Give the position of every Plasmodium parasite.
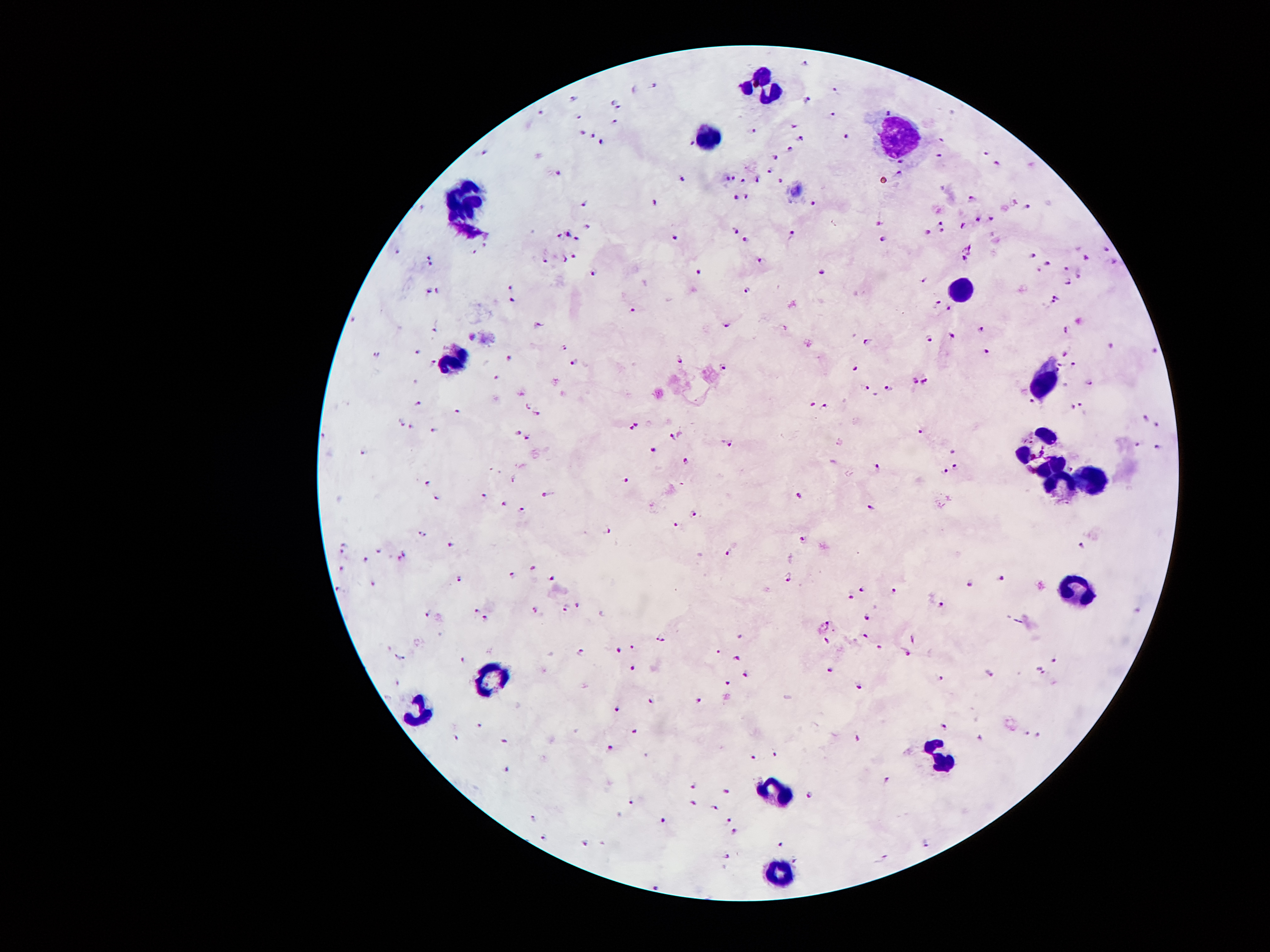

Approximate centers as {x, y} in pixels.
Plasmodium parasites: {805, 64}, {656, 86}, {635, 88}, {834, 89}, {575, 97}, {614, 100}, {808, 100}, {621, 108}, {541, 113}, {578, 114}, {834, 115}, {616, 120}, {583, 129}, {794, 129}, {752, 131}, {592, 134}, {847, 137}, {602, 141}, {801, 141}, {940, 141}, {692, 144}, {789, 151}, {486, 152}, {986, 154}, {776, 157}, {938, 157}, {997, 164}, {556, 170}, {771, 172}, {900, 173}, {727, 178}, {734, 178}, {757, 178}, {683, 180}, {743, 180}, {779, 181}, {747, 196}, {737, 199}, {971, 199}, {1013, 201}, {655, 202}, {420, 204}, {584, 204}, {811, 204}, {1025, 207}, {989, 218}, {977, 219}, {879, 223}, {939, 223}, {962, 225}, {585, 226}, {735, 227}, {924, 229}, {566, 231}, {939, 231}, {791, 232}, {556, 235}, {575, 237}, {675, 237}, {744, 238}, {882, 238}, {484, 243}, {1107, 247}, {398, 251}, {473, 251}, {1030, 254}, {574, 256}, {426, 257}, {541, 257}, {563, 257}, {963, 258}, {759, 259}, {1087, 259}, {1045, 263}, {427, 264}, {1066, 267}, {698, 270}, {821, 271}, {591, 272}, {1081, 276}, {921, 278}, {1070, 280}, {427, 290}, {436, 290}, {746, 290}, {1057, 295}, {512, 299}, {935, 301}, {1052, 303}, {948, 306}, {634, 310}, {352, 320}, {541, 326}, {728, 326}, {981, 328}, {1066, 328}, {435, 330}, {951, 335}, {930, 338}, {866, 341}, {1110, 346}, {565, 349}, {987, 350}, {419, 352}, {1154, 352}, {379, 354}, {1063, 355}, {510, 359}, {682, 359}, {433, 362}, {575, 362}, {1070, 366}, {1057, 367}, {724, 369}, {854, 369}, {1057, 370}, {498, 378}, {915, 380}, {923, 381}, {417, 382}, {1087, 383}, {865, 386}, {890, 388}, {877, 394}, {1032, 401}, {419, 403}, {813, 403}, {1078, 403}, {825, 404}, {1069, 406}, {527, 409}, {457, 410}, {537, 415}, {1145, 417}, {403, 421}, {638, 424}, {1158, 424}, {412, 426}, {631, 429}, {434, 431}, {921, 431}, {518, 433}, {673, 435}, {319, 436}, {528, 436}, {731, 442}, {1136, 443}, {1157, 447}, {655, 449}, {952, 451}, {362, 452}, {832, 460}, {688, 462}, {954, 464}, {877, 466}, {1070, 467}, {942, 470}, {625, 478}, {514, 480}, {428, 482}, {798, 493}, {484, 494}, {546, 494}, {438, 498}, {504, 503}, {870, 503}, {522, 508}, {695, 513}, {678, 523}, {607, 529}, {423, 531}, {802, 538}, {344, 544}, {452, 544}, {1081, 546}, {381, 549}, {342, 552}, {403, 553}, {728, 553}, {365, 558}, {398, 558}, {341, 567}, {534, 567}, {511, 576}, {792, 577}, {1000, 577}, {374, 578}, {552, 578}, {457, 579}, {968, 584}, {336, 587}, {864, 588}, {894, 591}, {849, 595}, {944, 603}, {578, 605}, {476, 607}, {566, 608}, {1138, 609}, {537, 610}, {428, 613}, {866, 616}, {486, 617}, {826, 626}, {865, 634}, {739, 636}, {913, 637}, {660, 639}, {826, 640}, {879, 645}, {632, 646}, {619, 650}, {716, 650}, {582, 651}, {906, 652}, {394, 655}, {735, 657}, {403, 658}, {464, 659}, {1054, 661}, {634, 666}, {830, 668}, {1039, 668}, {991, 672}, {744, 673}, {940, 676}, {398, 680}, {726, 682}, {860, 686}, {698, 698}, {650, 699}, {618, 709}, {479, 723}, {944, 725}, {633, 730}, {1028, 731}, {1040, 734}, {454, 736}, {980, 736}, {504, 739}, {855, 739}, {610, 746}, {773, 752}, {646, 753}, {752, 757}, {506, 768}, {886, 778}, {694, 785}, {725, 789}, {809, 793}, {629, 799}, {693, 802}, {714, 806}, {531, 816}, {728, 819}, {662, 820}, {736, 830}, {543, 836}, {584, 841}, {929, 841}, {780, 844}, {725, 855}, {796, 858}, {882, 858}, {656, 882}.

{
  "image_size": "1270×952 pixels",
  "preparation": "thick blood smear",
  "magnification": "100x",
  "leukocyte_locations": "approximate centers as {x, y} in pixels: {767, 80}, {704, 130}, {902, 136}, {467, 199}, {965, 285}, {456, 361}, {1049, 380}, {1045, 455}, {1095, 477}, {1061, 487}, {1074, 586}, {486, 678}, {425, 714}, {946, 762}, {778, 791}, {782, 873}",
  "patient_malaria_status": "positive for Plasmodium falciparum",
  "field_of_view": "one from this slide",
  "capture": "smartphone through the microscope eyepiece",
  "stain": "Giemsa"
}